State which cell type is depicted.
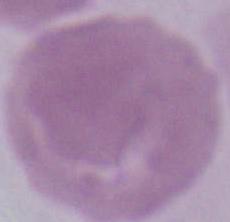

This is an erythrocyte.

Summary:
  - Modality: photomicrograph
  - Magnification: 1000x